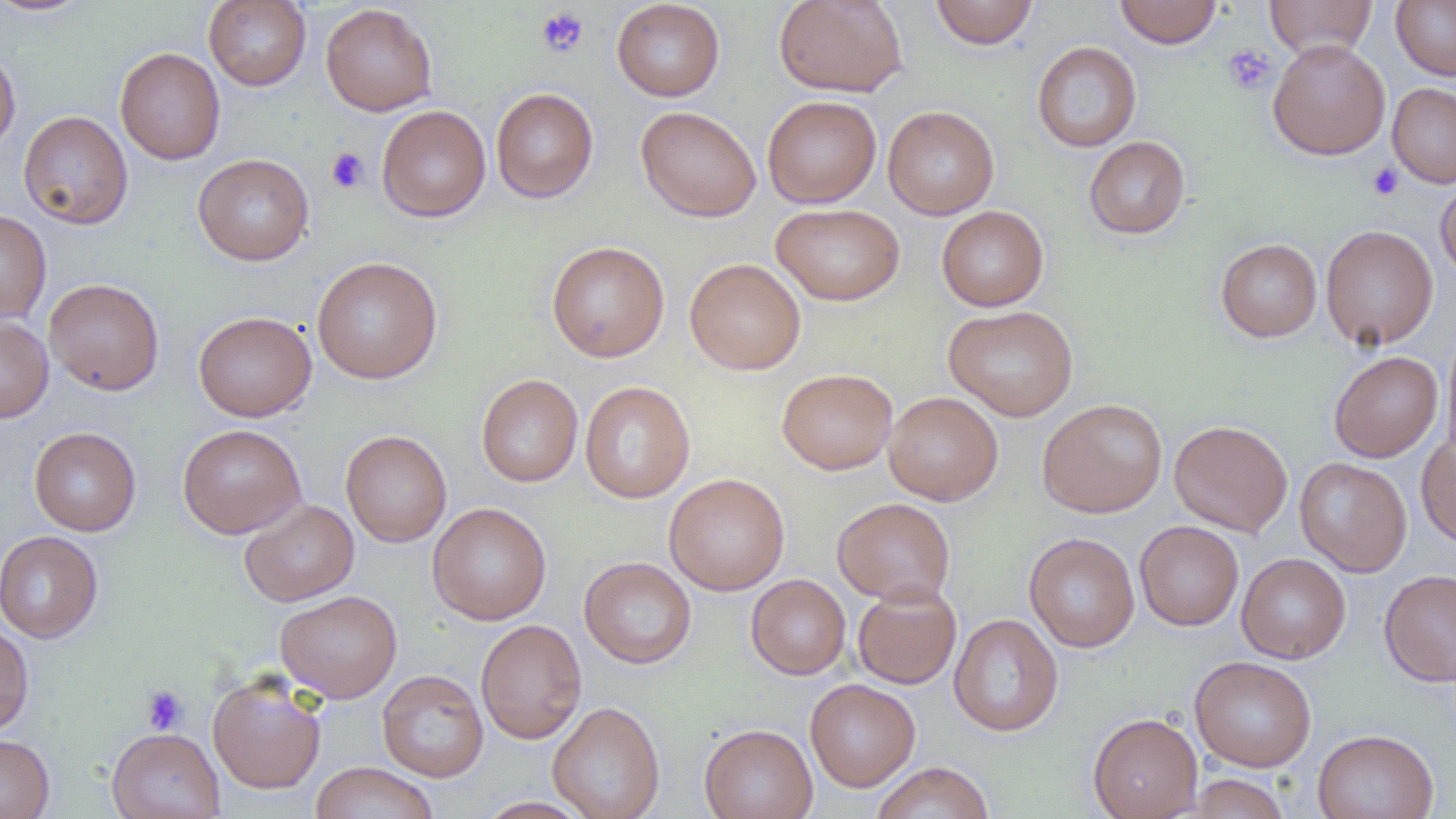

slide_level_diagnosis: no evidence of blood parasites
modality: light microscopy
image_size: 1456×819 pixels
field_of_view: one of a larger specimen
platelet_locations: 'approximate bounding boxes as (x1, y1, x2, y2) in pixels: (535, 7, 589, 59), (1222, 44, 1277, 96), (326, 147, 370, 194), (1367, 162, 1404, 201), (141, 684, 188, 735)'
preparation: thin blood smear
uninfected_red_blood_cell_locations: 'approximate bounding boxes as (x1, y1, x2, y2) in pixels: (0, 0, 96, 16), (773, 0, 908, 97), (1114, 0, 1223, 48), (1264, 0, 1377, 59), (1391, 0, 1456, 80), (204, 1, 311, 90), (611, 1, 725, 102), (930, 1, 1039, 49), (320, 4, 438, 116), (1267, 39, 1390, 159), (1032, 41, 1142, 152), (115, 47, 226, 165), (0, 49, 20, 154), (1387, 83, 1456, 188), (491, 87, 598, 203), (762, 95, 881, 208), (376, 104, 491, 222), (635, 105, 761, 222), (883, 105, 999, 220), (18, 110, 133, 229), (1084, 136, 1190, 239), (193, 153, 314, 265), (1436, 177, 1456, 282), (771, 203, 905, 306), (936, 205, 1049, 311), (0, 209, 52, 323), (1320, 224, 1438, 350), (1215, 238, 1322, 342), (546, 241, 670, 362), (312, 256, 443, 384), (684, 258, 806, 375), (44, 278, 164, 395), (943, 304, 1078, 422), (193, 310, 316, 422), (0, 316, 53, 423), (1441, 326, 1456, 463), (1329, 351, 1442, 462), (777, 368, 897, 475), (476, 373, 583, 487), (580, 381, 695, 503), (883, 391, 1003, 506), (1037, 397, 1168, 517), (1169, 419, 1293, 537), (177, 424, 306, 538), (29, 426, 141, 536), (341, 430, 452, 547), (1416, 433, 1456, 547), (1295, 457, 1412, 577), (663, 473, 790, 595), (832, 497, 956, 605), (239, 499, 359, 606), (427, 502, 552, 625), (1134, 521, 1244, 630), (0, 530, 103, 643), (1024, 532, 1140, 652), (1236, 553, 1351, 664), (579, 556, 696, 669), (1379, 569, 1456, 686), (746, 574, 850, 679), (852, 583, 962, 690), (275, 590, 402, 702), (949, 613, 1064, 736), (475, 619, 587, 744), (0, 622, 34, 736), (1189, 655, 1317, 772), (377, 669, 489, 782), (207, 671, 327, 795), (805, 678, 921, 792), (547, 700, 665, 819), (1088, 712, 1203, 819), (699, 723, 817, 819), (107, 727, 225, 818), (1313, 729, 1439, 819), (0, 734, 55, 819), (871, 761, 995, 819), (309, 762, 439, 819), (1186, 773, 1292, 818), (475, 797, 592, 818)'
magnification: 1000x